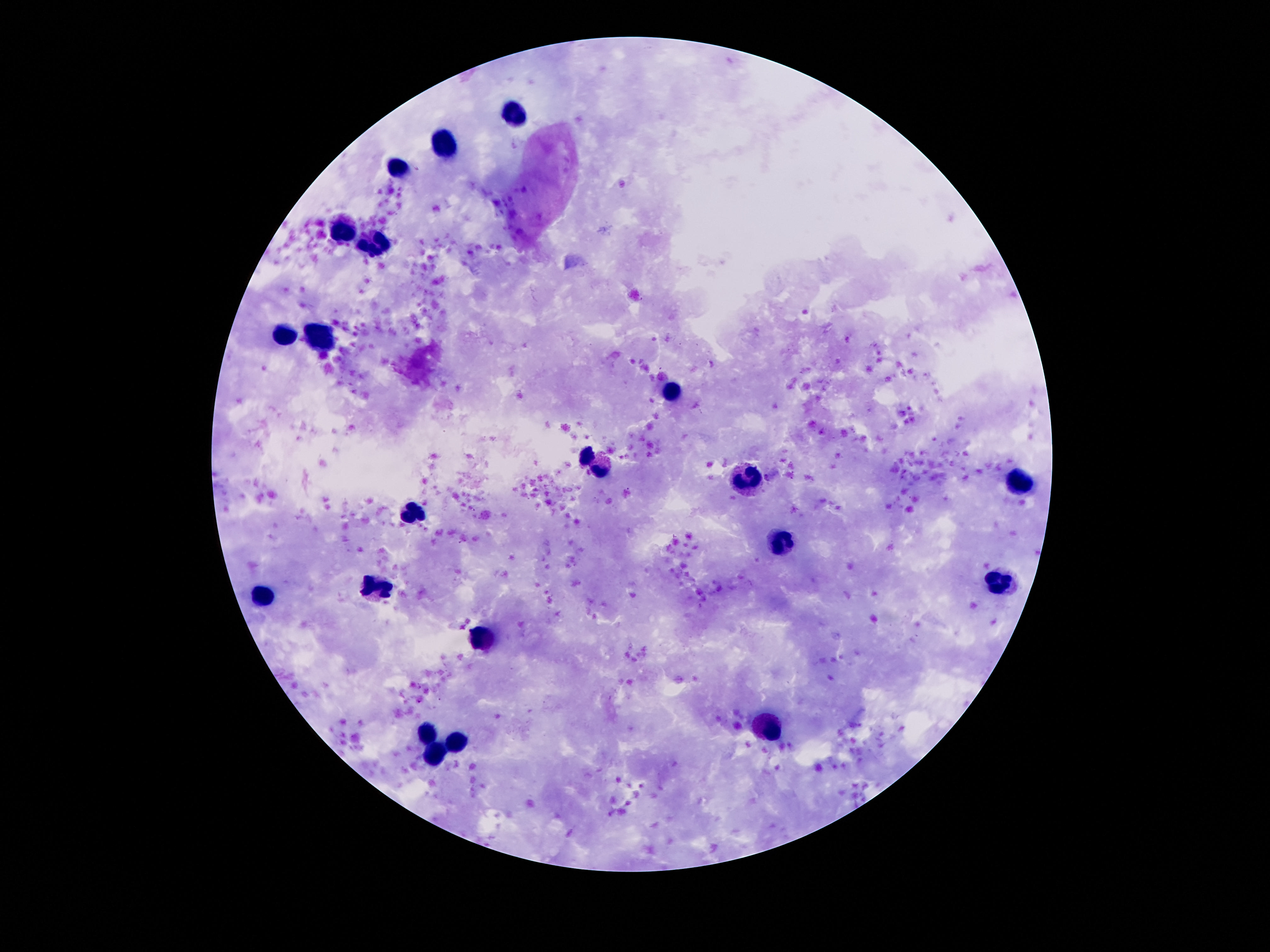
{
  "magnification": "100x",
  "stain": "Giemsa",
  "leukocyte_locations": "approximate centers as [x, y] in pixels: [512, 113], [444, 148], [398, 169], [344, 232], [378, 242], [283, 334], [321, 335], [669, 393], [585, 454], [601, 470], [746, 481], [1021, 482], [412, 513], [785, 543], [1000, 582], [374, 586], [262, 599], [480, 637], [764, 727], [426, 734], [453, 741], [437, 755]",
  "patient_malaria_status": "negative",
  "image_size": "1270×952 pixels",
  "field_of_view": "one from this slide",
  "capture": "smartphone camera through the microscope eyepiece",
  "preparation": "thick blood smear"
}